Assess this cell for malaria.
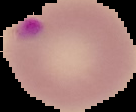
Parasitized.

Summary:
  - Preparation: thin blood film
  - Image size: 136×112 pixels
  - Image type: segmented cell region with the area outside set to black